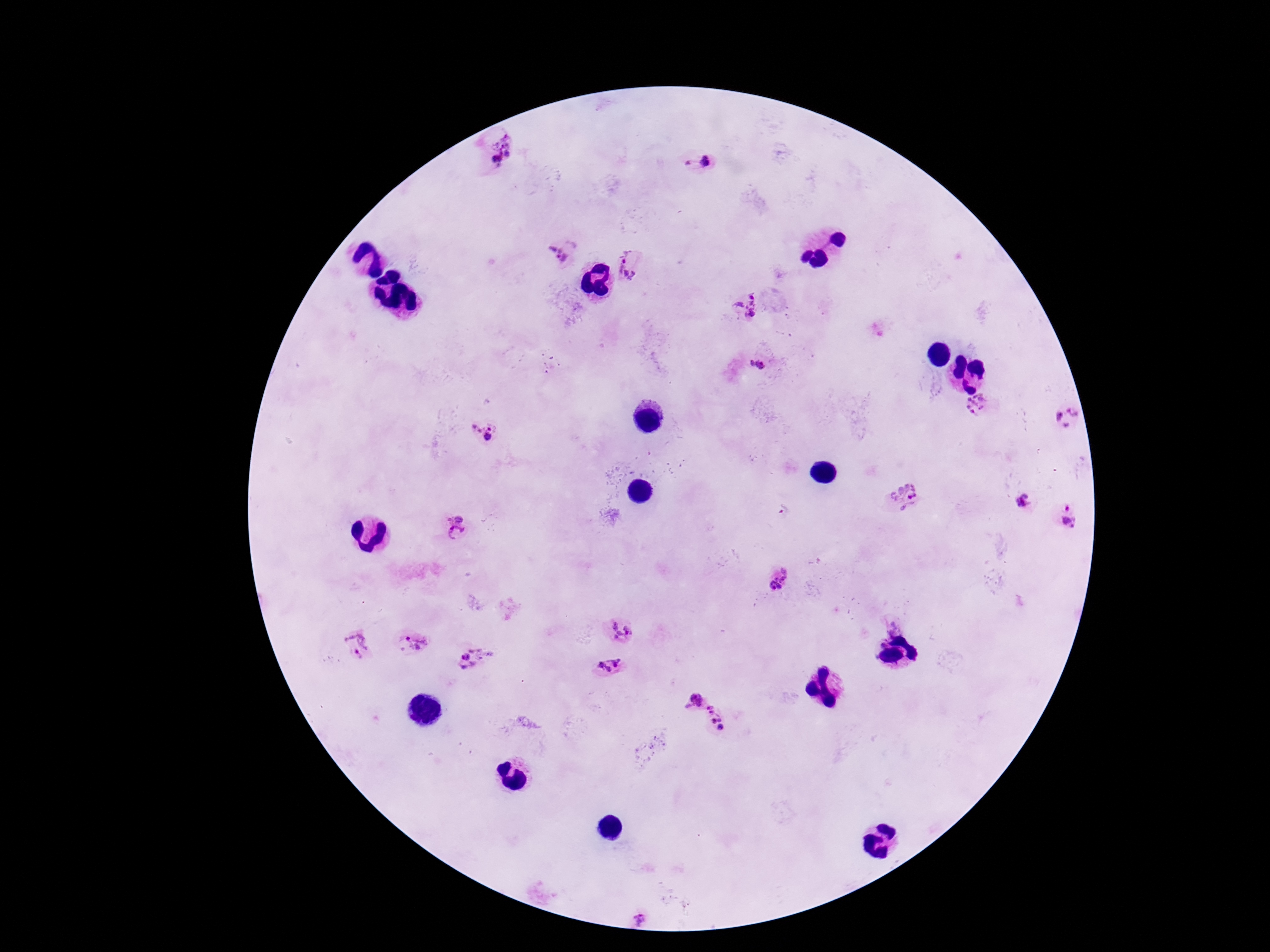

capture = smartphone camera through the microscope eyepiece
field of view = one from this slide
magnification = 100x
stain = Giemsa
patient malaria status = positive
preparation = thick peripheral-blood smear
Plasmodium parasite locations = approximate centers as [x, y] in pixels: [504, 156], [697, 161], [561, 252], [632, 264], [747, 305], [758, 365], [978, 404], [1065, 418], [483, 432], [905, 498], [1022, 504], [784, 510], [1066, 516], [455, 517], [456, 533], [776, 581], [893, 626], [621, 632], [411, 643], [881, 643], [358, 645], [474, 659], [609, 664], [692, 699], [718, 718]
image size = 1270×952 pixels